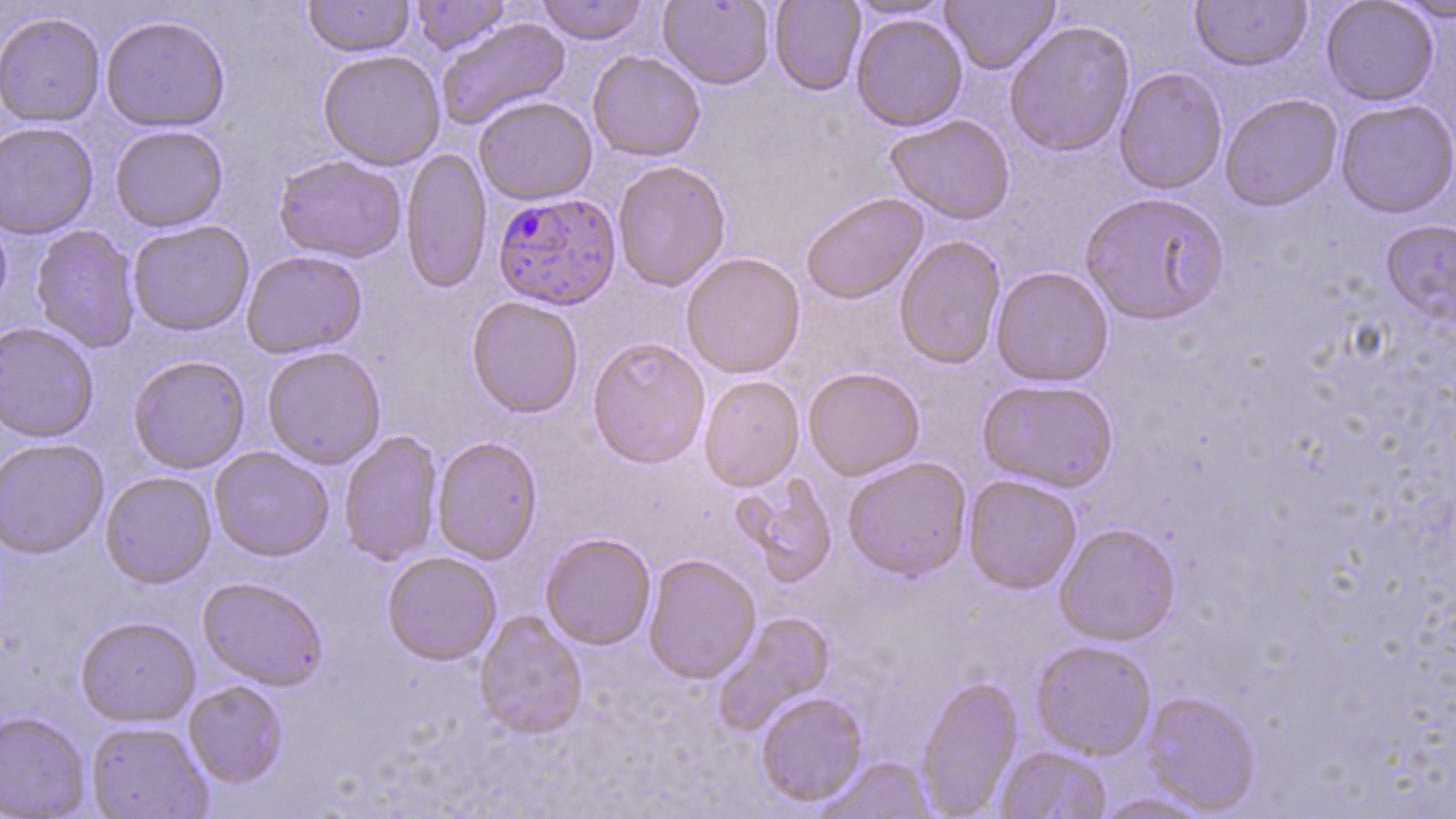 Approximate bounding boxes as [x1, y1, x2, y2] in pixels. Plasmodium falciparum-infected red blood cell locations: [493, 192, 621, 312]. Uninfected red blood cell locations: [303, 0, 415, 58], [410, 0, 511, 55], [536, 0, 649, 45], [658, 0, 774, 90], [843, 0, 955, 21], [940, 0, 1060, 74], [1190, 0, 1312, 72], [1389, 0, 1456, 24], [769, 1, 866, 96], [1321, 1, 1438, 106], [0, 13, 105, 128], [850, 13, 968, 132], [100, 16, 230, 134], [436, 17, 572, 131], [1003, 21, 1136, 158], [317, 50, 445, 171], [588, 51, 706, 162], [1114, 67, 1228, 195], [1220, 94, 1343, 212], [473, 97, 597, 206], [1335, 100, 1455, 219], [885, 115, 1015, 225], [0, 123, 98, 240], [109, 126, 228, 233], [400, 148, 491, 295], [273, 156, 407, 264], [612, 161, 731, 293], [1080, 193, 1230, 327], [801, 194, 928, 306], [0, 210, 12, 320], [1380, 220, 1456, 328], [127, 221, 254, 337], [30, 225, 140, 353], [894, 236, 1006, 371], [241, 251, 367, 360], [681, 253, 806, 379], [991, 268, 1114, 387], [466, 298, 583, 420], [0, 323, 99, 444], [588, 340, 710, 470], [262, 347, 386, 470], [128, 356, 251, 475], [803, 368, 925, 481], [698, 376, 805, 492], [977, 380, 1119, 493], [338, 430, 444, 567], [432, 437, 543, 565], [0, 439, 109, 559], [209, 447, 334, 562], [842, 457, 971, 582], [100, 472, 216, 589], [730, 472, 838, 587], [963, 475, 1082, 594], [1054, 524, 1181, 646], [540, 533, 656, 651], [382, 551, 501, 667], [643, 555, 761, 685], [197, 577, 328, 691], [473, 611, 588, 741], [712, 612, 837, 735], [75, 617, 200, 728], [1030, 641, 1156, 760], [918, 674, 1023, 816], [184, 681, 288, 788], [755, 692, 869, 808], [1140, 692, 1261, 815], [0, 712, 90, 819], [85, 721, 212, 819], [994, 746, 1111, 819], [816, 756, 937, 818], [1089, 792, 1218, 818]. Slide-level diagnosis: Plasmodium falciparum. Optical microscopy. 1000x magnification. Thin blood smear. May-Grünwald-Giemsa stain. Image is 1456×819 pixels. Single field of view.